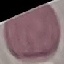
Summary:
  - Result: no malaria parasites seen
  - Image type: automatically extracted cell patch, resized to 64 × 64 pixels
  - Stain: Giemsa
  - Capture: smartphone through the microscope eyepiece
  - Preparation: thin blood film